Give the extent of all uninfected red blood cells.
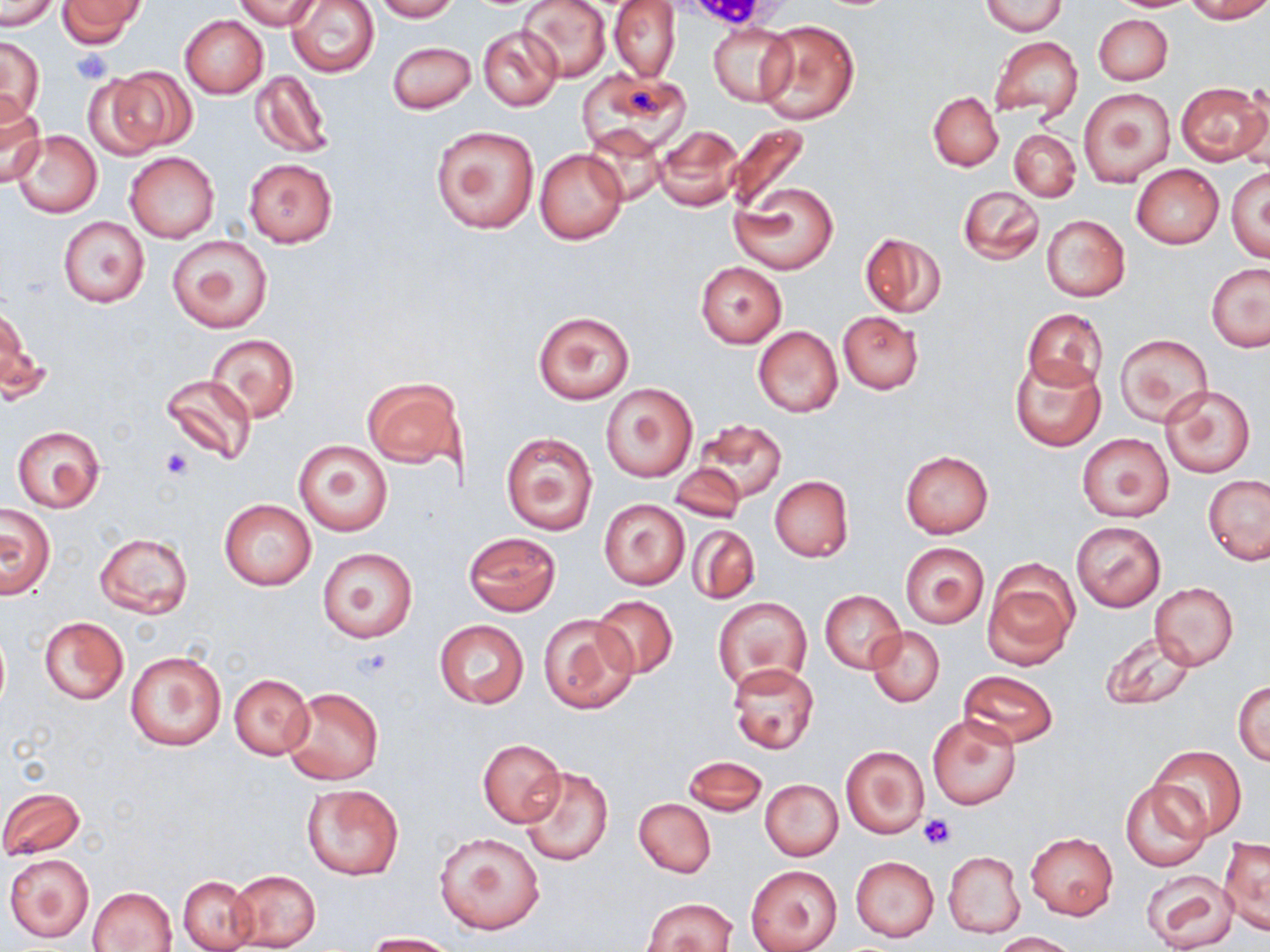

Approximate bounding boxes as (x1,y1)-(x2,y2) corner pairs in pixels.
Uninfected red blood cells: (0,0)-(57,29), (234,0)-(321,29), (286,0)-(379,76), (373,0)-(459,21), (610,0)-(680,82), (1105,0)-(1200,12), (1186,0)-(1270,22), (57,1)-(145,45), (519,1)-(610,81), (978,1)-(1066,35), (180,15)-(268,98), (1093,15)-(1172,85), (755,18)-(858,126), (707,23)-(795,105), (478,25)-(563,111), (1,36)-(46,125), (989,37)-(1082,120), (387,41)-(476,114), (105,68)-(196,153), (578,68)-(694,158), (251,71)-(331,157), (1175,81)-(1270,167), (1079,88)-(1175,187), (928,92)-(1002,171), (1,102)-(46,186), (431,124)-(539,234), (654,124)-(747,214), (723,124)-(812,217), (1010,129)-(1080,201), (12,130)-(103,218), (534,147)-(628,244), (125,151)-(219,243), (244,158)-(337,247), (1131,164)-(1224,249), (1227,168)-(1270,262), (731,182)-(840,275), (956,185)-(1044,263), (1040,214)-(1129,302), (57,215)-(150,308), (166,233)-(273,334), (862,233)-(946,319), (695,262)-(787,347), (1206,263)-(1270,352), (0,308)-(37,402), (1022,308)-(1107,391), (533,310)-(633,405), (837,311)-(924,393), (752,325)-(843,417), (1116,334)-(1215,428), (207,335)-(300,422), (1008,352)-(1107,451), (161,372)-(258,464), (361,376)-(467,473), (600,382)-(697,483), (1160,385)-(1255,478), (693,419)-(788,504), (11,426)-(104,512), (501,431)-(598,536), (1078,433)-(1174,521), (292,438)-(393,536), (899,450)-(995,539), (670,464)-(747,525), (1203,474)-(1270,563), (769,475)-(854,562), (219,498)-(316,590), (599,499)-(689,589), (0,504)-(56,599), (1071,521)-(1166,611), (689,525)-(760,603), (94,531)-(192,617), (464,532)-(560,615), (900,542)-(988,628), (318,548)-(417,642), (982,567)-(1076,669), (1150,583)-(1238,670), (821,591)-(904,673), (590,595)-(678,679), (712,595)-(812,691), (539,615)-(639,714), (38,616)-(128,705), (434,619)-(529,708), (866,626)-(944,706), (1099,630)-(1198,712), (125,650)-(227,751), (725,662)-(820,756), (958,670)-(1057,748), (228,673)-(313,760), (1233,681)-(1270,764), (282,685)-(385,786), (926,713)-(1022,810), (478,738)-(567,828), (840,746)-(929,838), (1151,746)-(1247,838), (682,756)-(768,816), (518,765)-(614,866), (760,779)-(842,861), (1120,779)-(1212,871), (301,783)-(405,881), (0,787)-(86,858), (633,798)-(716,877), (434,831)-(545,935), (1026,832)-(1119,920), (1217,838)-(1270,932), (943,850)-(1024,938), (4,853)-(95,944), (849,855)-(939,942), (746,865)-(841,952), (1140,868)-(1237,952), (228,869)-(322,952), (178,876)-(256,952), (87,887)-(176,951), (642,897)-(738,952), (362,931)-(459,951), (993,931)-(1079,952).

Summary:
  - Platelet locations: (71,48)-(113,85), (626,91)-(662,116), (160,447)-(194,479), (352,648)-(391,679), (918,813)-(957,850)
  - Slide-level diagnosis: negative for blood parasites
  - Image size: 1270×952 pixels
  - Field of view: one of a larger specimen
  - Preparation: thin blood smear
  - Magnification: 1000x
  - Modality: optical microscopy
  - Stain: May-Grünwald-Giemsa